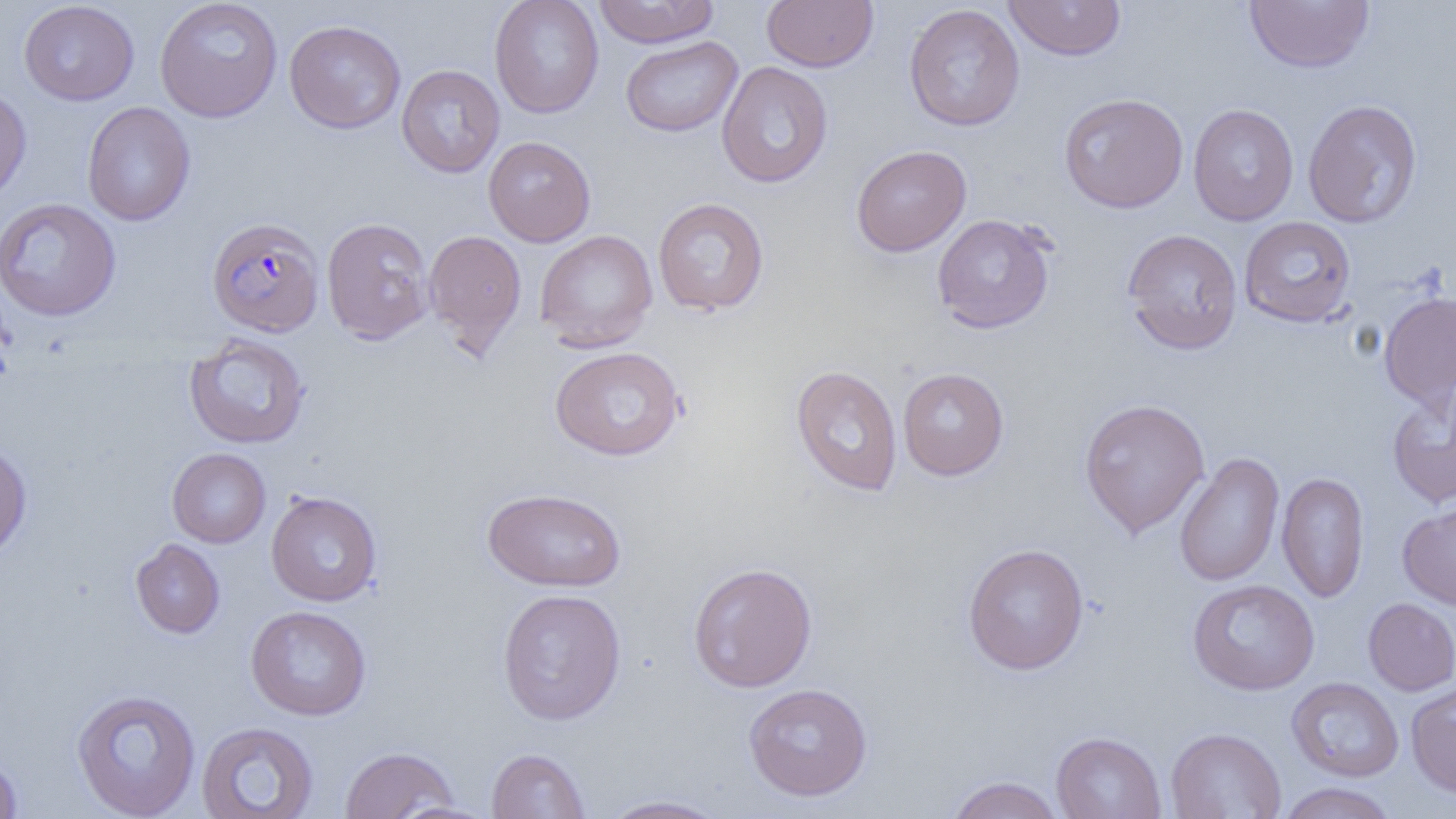

slide-level diagnosis = Plasmodium falciparum
magnification = 1000x
image size = 1456×819 pixels
Plasmodium falciparum-infected red blood cell locations = approximate bounding boxes as named x1/y1/x2/y2 corners in pixels: (x1=206, y1=218, x2=326, y2=338)
field of view = single
uninfected red blood cell locations = approximate bounding boxes as named x1/y1/x2/y2 corners in pixels: (x1=154, y1=0, x2=283, y2=123), (x1=489, y1=0, x2=604, y2=118), (x1=593, y1=0, x2=719, y2=48), (x1=762, y1=0, x2=879, y2=72), (x1=1003, y1=0, x2=1127, y2=61), (x1=18, y1=1, x2=139, y2=105), (x1=1244, y1=1, x2=1374, y2=73), (x1=903, y1=4, x2=1025, y2=131), (x1=283, y1=20, x2=406, y2=135), (x1=620, y1=35, x2=743, y2=137), (x1=716, y1=60, x2=833, y2=189), (x1=396, y1=64, x2=505, y2=178), (x1=0, y1=83, x2=32, y2=205), (x1=1058, y1=93, x2=1188, y2=214), (x1=1303, y1=99, x2=1423, y2=229), (x1=82, y1=102, x2=195, y2=226), (x1=1187, y1=103, x2=1299, y2=226), (x1=483, y1=136, x2=596, y2=246), (x1=851, y1=145, x2=971, y2=257), (x1=652, y1=197, x2=769, y2=316), (x1=0, y1=198, x2=121, y2=321), (x1=932, y1=213, x2=1056, y2=334), (x1=1239, y1=216, x2=1356, y2=327), (x1=321, y1=217, x2=435, y2=345), (x1=1122, y1=228, x2=1243, y2=355), (x1=423, y1=229, x2=527, y2=355), (x1=534, y1=229, x2=658, y2=352), (x1=1378, y1=291, x2=1456, y2=409), (x1=184, y1=333, x2=310, y2=449), (x1=549, y1=346, x2=686, y2=461), (x1=790, y1=364, x2=903, y2=497), (x1=898, y1=367, x2=1009, y2=481), (x1=1386, y1=387, x2=1456, y2=508), (x1=1078, y1=397, x2=1210, y2=538), (x1=0, y1=440, x2=32, y2=562), (x1=167, y1=448, x2=270, y2=548), (x1=1174, y1=452, x2=1284, y2=588), (x1=1276, y1=471, x2=1370, y2=602), (x1=482, y1=487, x2=627, y2=592), (x1=266, y1=491, x2=382, y2=606), (x1=1397, y1=501, x2=1456, y2=610), (x1=131, y1=538, x2=224, y2=639), (x1=962, y1=543, x2=1090, y2=675), (x1=688, y1=562, x2=818, y2=693), (x1=1187, y1=578, x2=1320, y2=696), (x1=497, y1=588, x2=627, y2=725), (x1=1363, y1=597, x2=1456, y2=696), (x1=246, y1=605, x2=371, y2=720), (x1=1286, y1=677, x2=1404, y2=782), (x1=1406, y1=681, x2=1456, y2=798), (x1=742, y1=682, x2=873, y2=801), (x1=71, y1=688, x2=201, y2=818), (x1=195, y1=721, x2=319, y2=818), (x1=1165, y1=727, x2=1286, y2=818), (x1=1051, y1=731, x2=1167, y2=818), (x1=339, y1=745, x2=460, y2=818), (x1=486, y1=747, x2=591, y2=818), (x1=0, y1=752, x2=22, y2=818), (x1=946, y1=775, x2=1065, y2=819), (x1=1276, y1=782, x2=1399, y2=819), (x1=598, y1=794, x2=731, y2=818), (x1=390, y1=801, x2=500, y2=819)
modality = optical microscopy
preparation = thin blood film